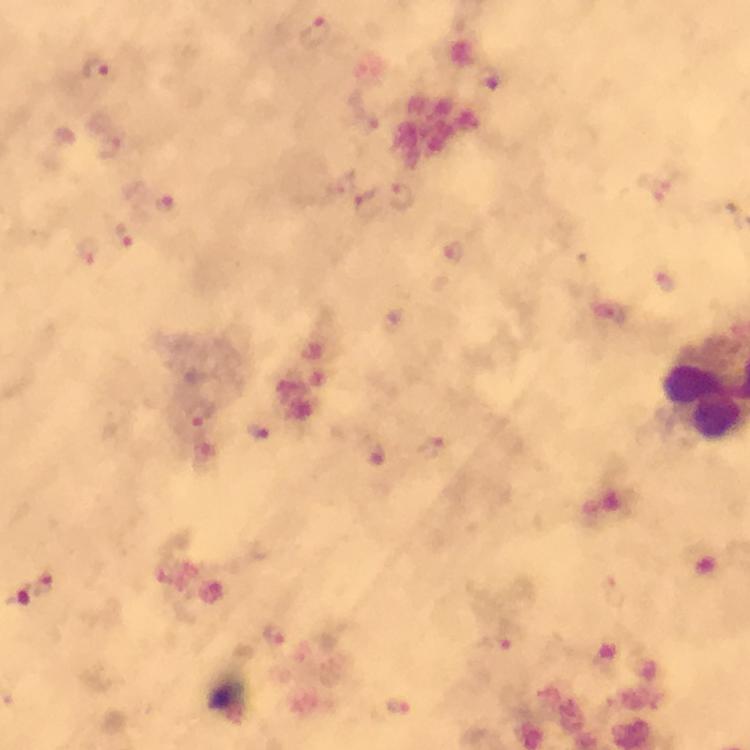
image_size: 750×750 pixels
immersion_oil: used
context: from a diagnostic examination for malaria
capture: smartphone photograph through a microscope
preparation: thick blood film
magnification: 100x
malaria_parasite_locations: 'approximate centers as [x, y] in pixels: [315, 33], [98, 68], [488, 79], [112, 147], [404, 197], [368, 203], [165, 205], [126, 236], [455, 252], [89, 254], [662, 283], [200, 415], [257, 432], [44, 582], [20, 595], [274, 634], [493, 645], [399, 707]'
stain: Giemsa
cropped_from: one field of view